Comment on the morphology of the erythrocytes.
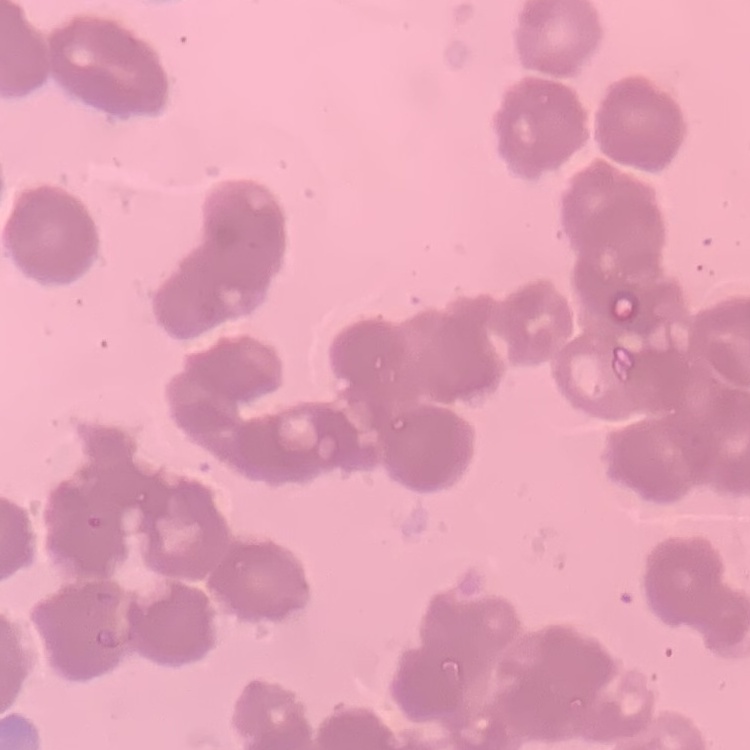

Rouleaux formation.

{
  "image_type": "one tile cut from a larger photomicrograph",
  "stain": "Field's or Giemsa",
  "preparation": "thin peripheral smear"
}